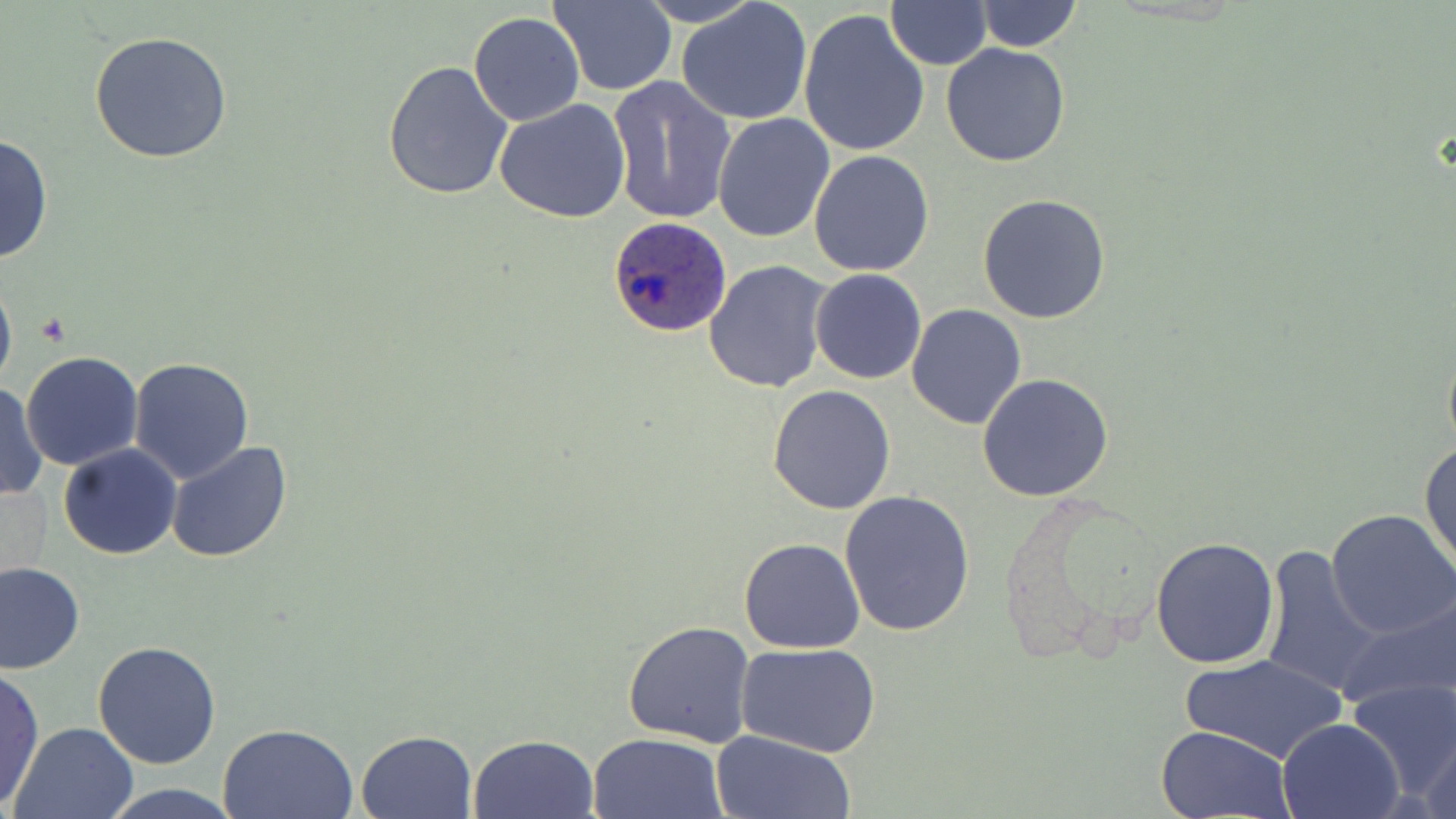

slide-level diagnosis = Plasmodium ovale
field of view = single
uninfected red blood cell locations = approximate bounding boxes as [x1, y1, x2, y2] in pixels: [547, 0, 677, 96], [633, 0, 765, 27], [678, 0, 813, 126], [974, 0, 1083, 53], [886, 3, 993, 68], [799, 10, 931, 161], [468, 12, 585, 126], [89, 30, 233, 163], [940, 43, 1071, 167], [383, 59, 513, 199], [607, 75, 736, 227], [493, 98, 632, 224], [712, 114, 836, 243], [0, 132, 53, 268], [808, 149, 936, 278], [977, 192, 1110, 325], [703, 260, 835, 395], [0, 264, 17, 402], [810, 268, 926, 385], [906, 303, 1029, 429], [1441, 331, 1456, 464], [21, 351, 143, 471], [128, 357, 255, 483], [977, 372, 1115, 502], [0, 382, 48, 503], [767, 385, 896, 515], [1419, 438, 1455, 576], [165, 442, 294, 564], [58, 444, 182, 560], [838, 489, 974, 636], [1327, 510, 1456, 642], [1150, 535, 1279, 669], [739, 537, 867, 654], [1259, 545, 1382, 699], [0, 562, 84, 674], [1334, 591, 1456, 716], [623, 620, 755, 748], [93, 641, 222, 769], [737, 641, 883, 758], [1182, 653, 1345, 764], [0, 667, 46, 809], [1348, 678, 1456, 806], [1278, 717, 1404, 818], [8, 721, 139, 818], [217, 722, 359, 819], [1156, 724, 1295, 818], [1417, 727, 1456, 819], [357, 729, 476, 817], [710, 730, 855, 818], [587, 731, 728, 819], [467, 733, 598, 818], [99, 782, 242, 819]
stain = May-Grünwald-Giemsa
Plasmodium ovale-infected red blood cell locations = approximate bounding boxes as [x1, y1, x2, y2] in pixels: [606, 216, 731, 337]
modality = optical microscopy
preparation = thin blood film
magnification = 1000x
image size = 1456×819 pixels